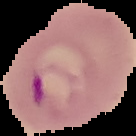
image_size: 136×136 pixels
image_type: segmented cell region on a black background
malaria_status: parasitized
preparation: thin blood smear